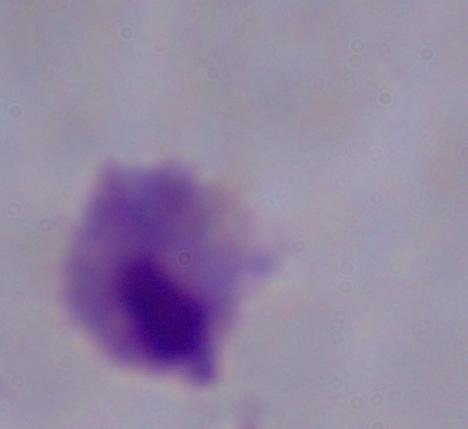
Summary:
  - Magnification: 1000x
  - Identification: trichomonad
  - Modality: photomicrograph